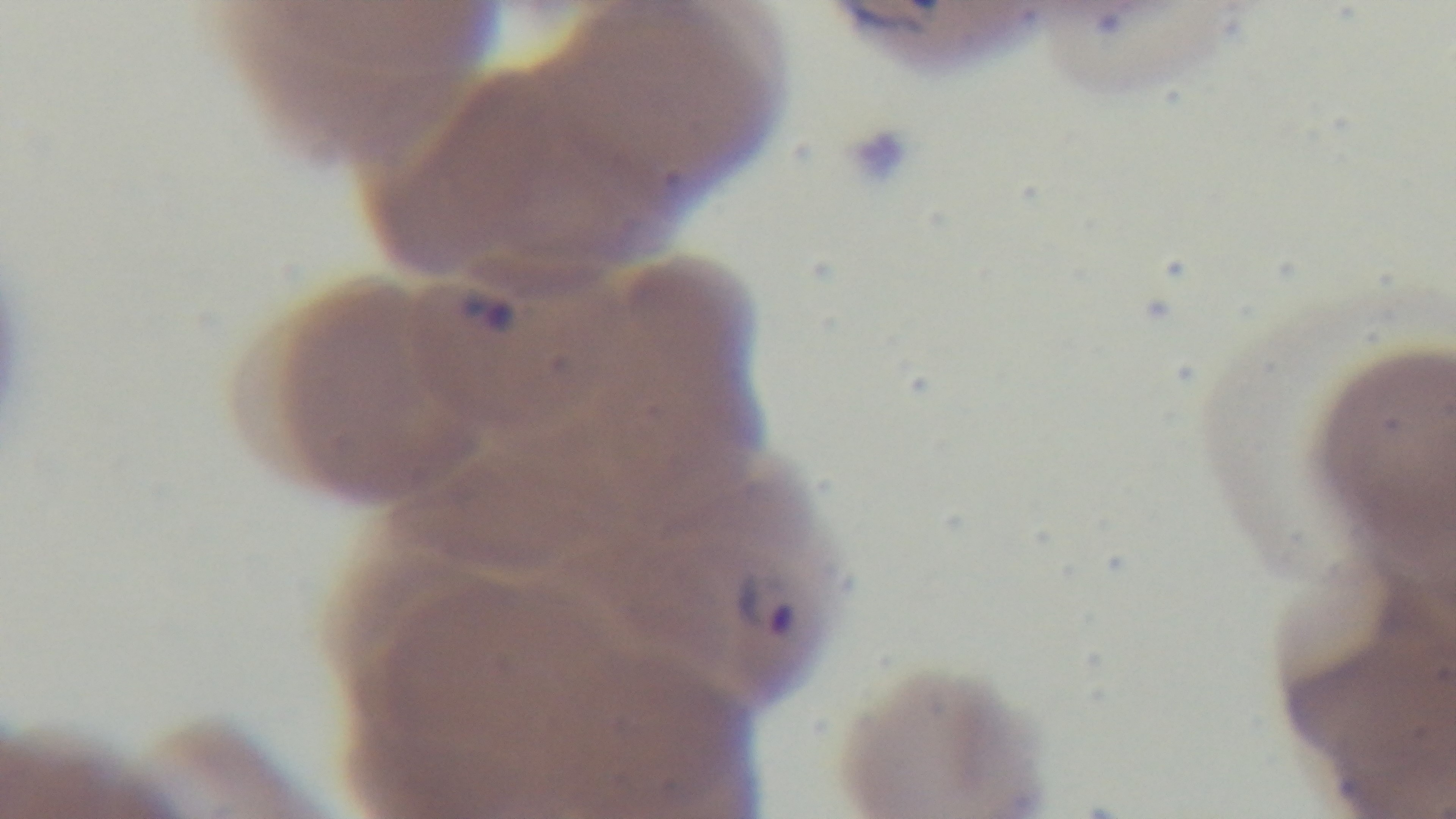 Single field of view. Mounted 4K digital camera. Photomicrograph. Preparation: thin smear. Malaria status: infected. Oil-immersion objective, 100x. Giemsa stain.